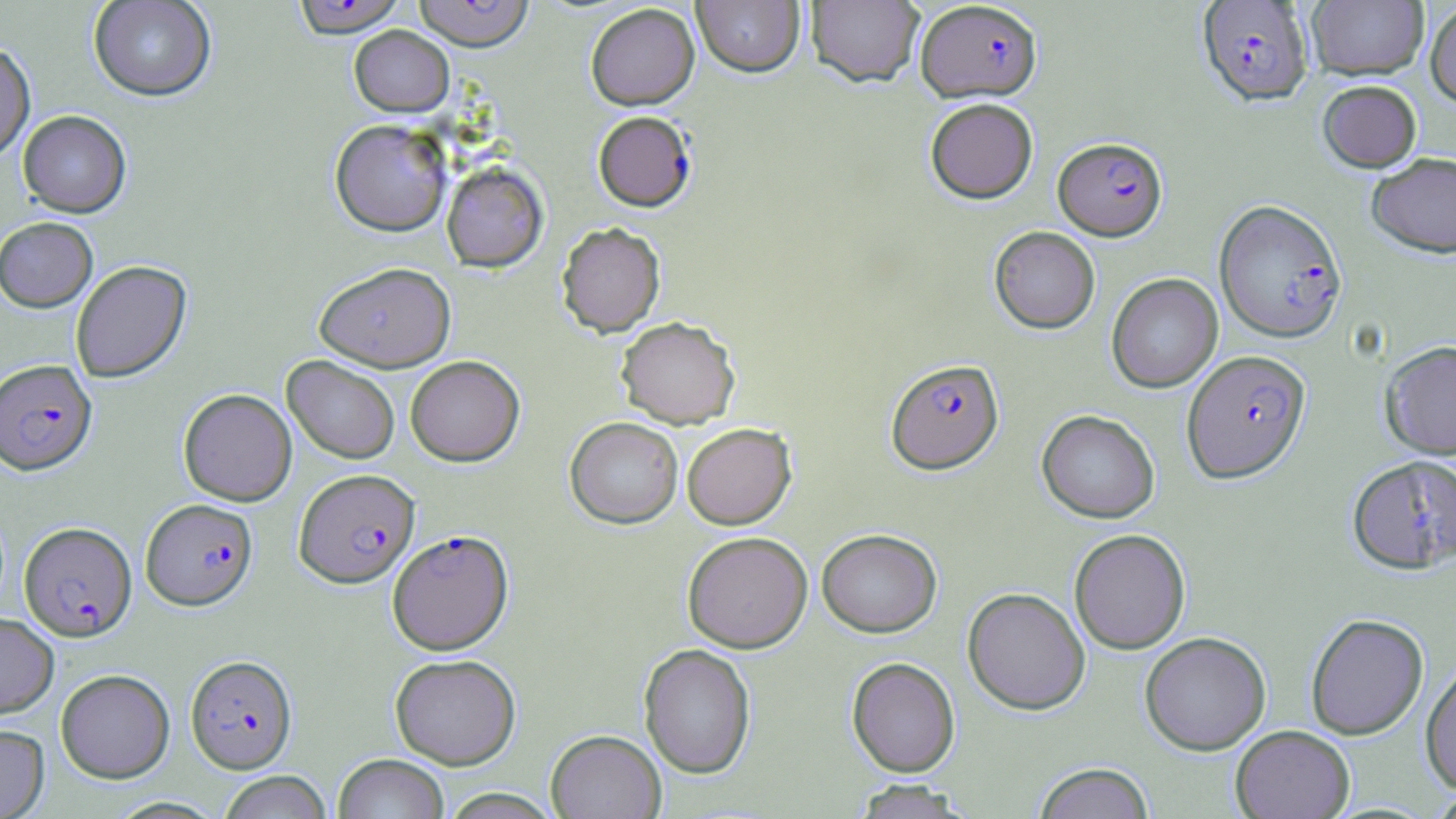
{
  "slide_level_diagnosis": "Plasmodium falciparum",
  "magnification": "1000x",
  "field_of_view": "one of a larger specimen",
  "preparation": "thin blood film",
  "modality": "optical microscopy",
  "plasmodium_falciparum_infected_red_blood_cell_locations": "approximate bounding boxes as [x1, y1, x2, y2] in pixels: [290, 0, 407, 37], [413, 1, 534, 51], [915, 1, 1043, 103], [1196, 1, 1313, 106], [592, 111, 696, 212], [1053, 136, 1167, 240], [1214, 200, 1347, 343], [1181, 350, 1311, 483], [886, 358, 1003, 474], [0, 359, 96, 474], [294, 468, 420, 587], [141, 498, 257, 610], [20, 521, 137, 640], [387, 529, 513, 654], [185, 655, 297, 773]",
  "image_size": "1456×819 pixels",
  "uninfected_red_blood_cell_locations": "approximate bounding boxes as [x1, y1, x2, y2] in pixels: [88, 0, 217, 101], [806, 0, 925, 88], [692, 1, 805, 77], [1307, 1, 1428, 80], [1425, 2, 1456, 106], [585, 4, 700, 110], [349, 25, 454, 117], [0, 41, 36, 163], [1317, 80, 1422, 172], [925, 97, 1038, 203], [18, 110, 131, 217], [329, 119, 452, 237], [1366, 152, 1456, 258], [441, 161, 549, 272], [0, 216, 98, 312], [556, 222, 666, 338], [989, 226, 1100, 333], [70, 260, 192, 383], [314, 262, 455, 371], [1106, 273, 1223, 393], [616, 316, 740, 428], [1380, 340, 1456, 459], [282, 355, 400, 464], [405, 355, 524, 466], [178, 388, 297, 506], [1037, 410, 1160, 523], [565, 416, 683, 529], [682, 422, 796, 529], [1346, 454, 1455, 573], [817, 528, 942, 637], [1069, 529, 1190, 654], [682, 531, 812, 653], [962, 587, 1090, 714], [0, 613, 58, 719], [1305, 613, 1428, 740], [1139, 631, 1271, 755], [639, 643, 756, 779], [390, 653, 520, 769], [846, 657, 960, 777], [1420, 659, 1456, 794], [56, 668, 175, 783], [0, 725, 49, 818], [1230, 725, 1355, 819], [546, 729, 666, 819], [334, 753, 449, 819], [1032, 762, 1155, 818], [216, 771, 333, 819], [849, 780, 973, 818], [438, 788, 564, 818]",
  "stain": "May-Grünwald-Giemsa"
}